Assess for malaria.
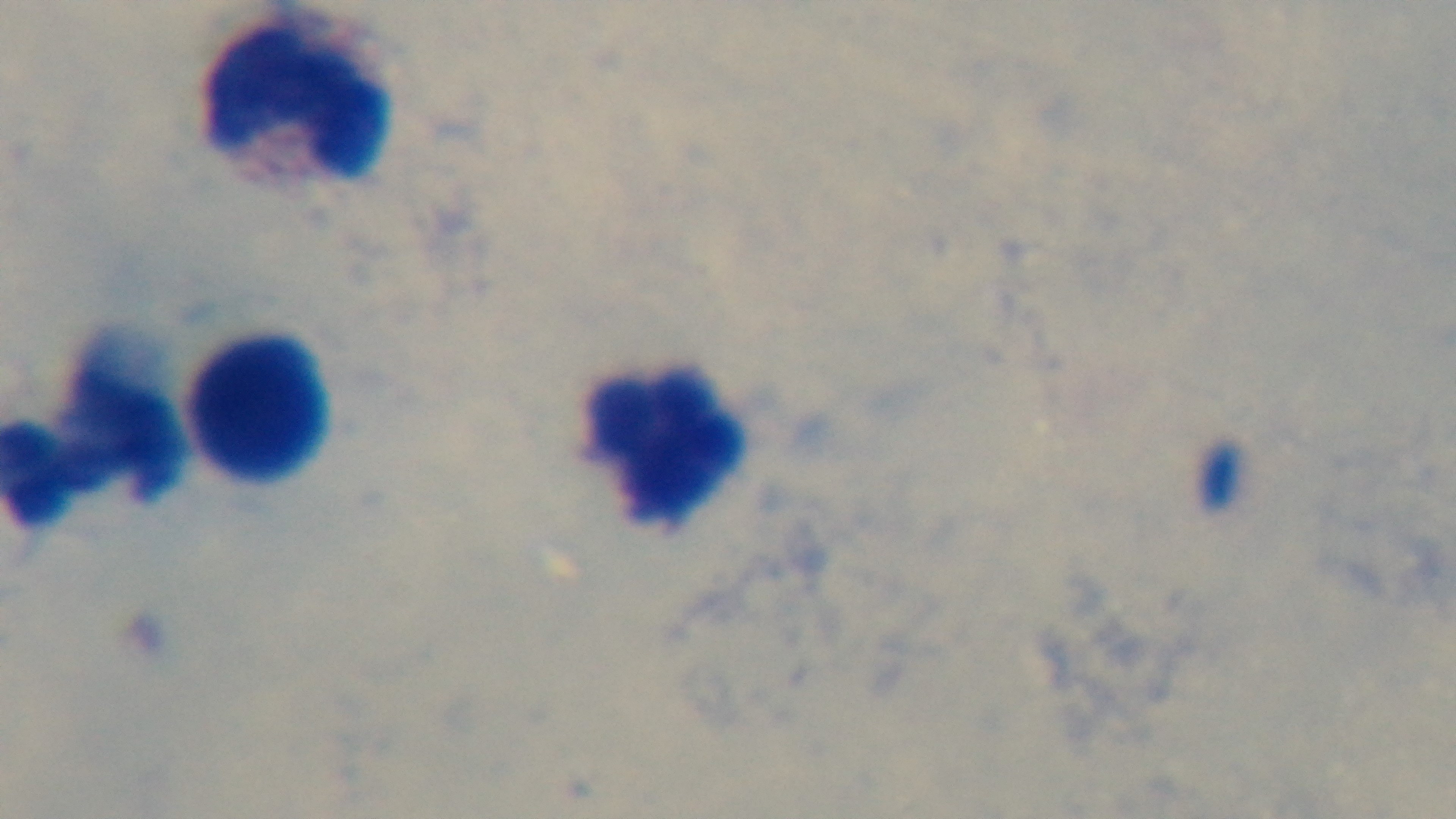
Uninfected.

Photomicrograph. Mounted 4K digital camera. Oil-immersion objective, 100x. Giemsa-stained. One field from the slide. Preparation: thick.